Locate and identify every blood parasite.
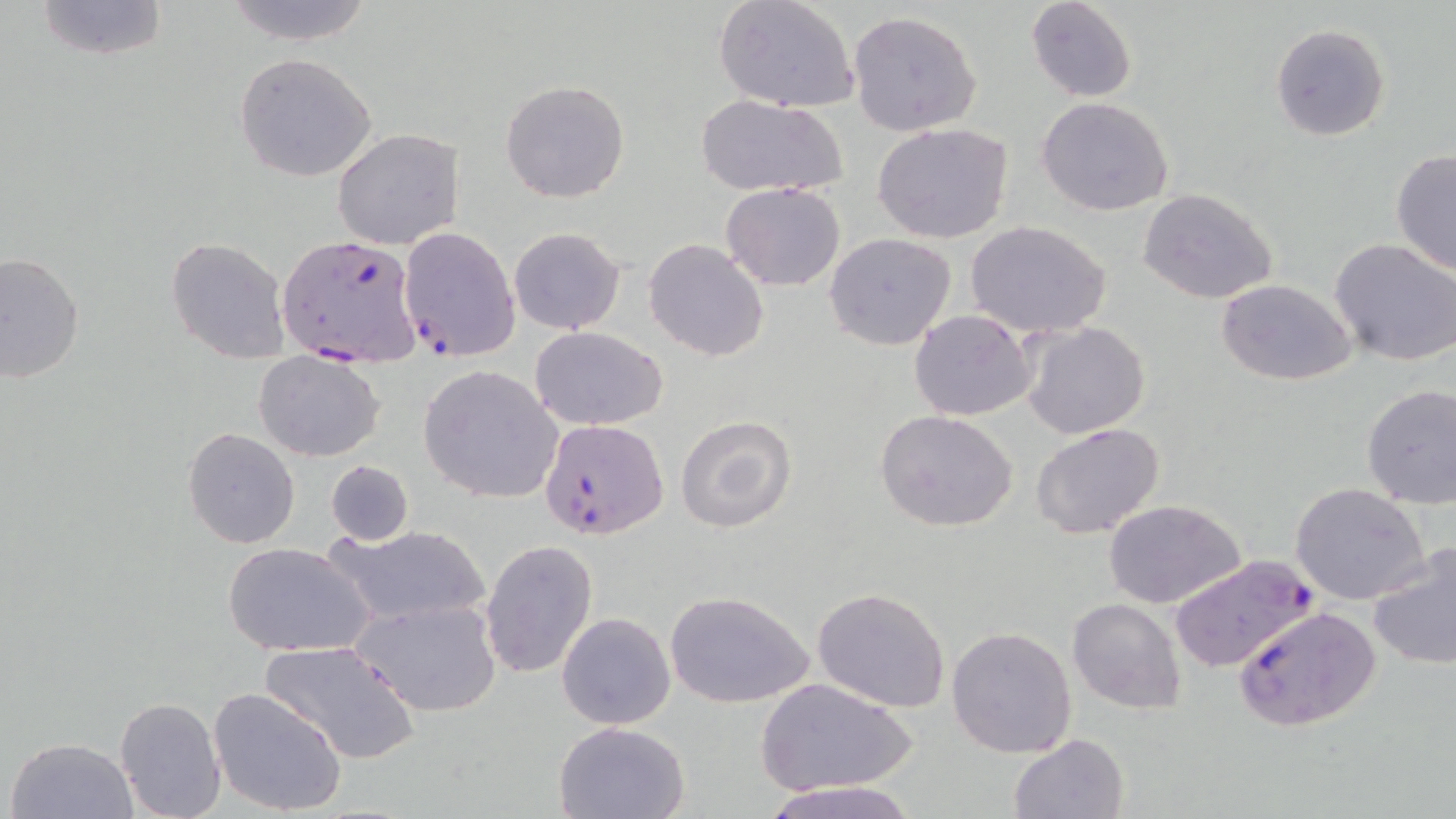
Approximate bounding boxes as named x1/y1/x2/y2 corners in pixels.
Plasmodium falciparum-infected red blood cells: (x1=397, y1=226, x2=520, y2=359), (x1=275, y1=235, x2=419, y2=360), (x1=540, y1=418, x2=669, y2=541), (x1=1167, y1=555, x2=1313, y2=673), (x1=1233, y1=604, x2=1382, y2=736).
No Plasmodium ovale, Plasmodium malariae, Plasmodium vivax, Babesia divergens, or Trypanosoma brucei observed.

Uninfected red blood cell locations: (x1=32, y1=0, x2=169, y2=61), (x1=219, y1=0, x2=379, y2=46), (x1=1025, y1=0, x2=1138, y2=102), (x1=715, y1=1, x2=860, y2=113), (x1=848, y1=10, x2=983, y2=135), (x1=1270, y1=23, x2=1391, y2=140), (x1=233, y1=52, x2=378, y2=182), (x1=500, y1=80, x2=630, y2=203), (x1=696, y1=95, x2=847, y2=199), (x1=1036, y1=96, x2=1174, y2=216), (x1=872, y1=124, x2=1015, y2=245), (x1=332, y1=127, x2=463, y2=248), (x1=1390, y1=150, x2=1455, y2=275), (x1=721, y1=182, x2=845, y2=291), (x1=1136, y1=188, x2=1281, y2=307), (x1=965, y1=219, x2=1113, y2=340), (x1=509, y1=227, x2=626, y2=335), (x1=825, y1=233, x2=958, y2=351), (x1=166, y1=236, x2=290, y2=363), (x1=1329, y1=238, x2=1456, y2=368), (x1=644, y1=239, x2=768, y2=361), (x1=0, y1=252, x2=84, y2=387), (x1=1215, y1=279, x2=1359, y2=385), (x1=908, y1=310, x2=1037, y2=421), (x1=1019, y1=320, x2=1151, y2=440), (x1=531, y1=327, x2=668, y2=430), (x1=255, y1=352, x2=384, y2=460), (x1=420, y1=365, x2=565, y2=504), (x1=1360, y1=384, x2=1456, y2=509), (x1=874, y1=409, x2=1021, y2=534), (x1=675, y1=415, x2=797, y2=532), (x1=1031, y1=421, x2=1166, y2=539), (x1=183, y1=427, x2=300, y2=548), (x1=325, y1=459, x2=412, y2=547), (x1=1290, y1=483, x2=1430, y2=605), (x1=1103, y1=498, x2=1248, y2=607), (x1=329, y1=524, x2=490, y2=627), (x1=479, y1=539, x2=598, y2=679), (x1=1368, y1=539, x2=1456, y2=671), (x1=223, y1=542, x2=375, y2=658), (x1=810, y1=587, x2=952, y2=714), (x1=664, y1=590, x2=813, y2=710), (x1=353, y1=597, x2=502, y2=716), (x1=1067, y1=598, x2=1186, y2=715), (x1=556, y1=611, x2=677, y2=730), (x1=946, y1=626, x2=1078, y2=759), (x1=260, y1=638, x2=420, y2=764), (x1=754, y1=675, x2=918, y2=796), (x1=208, y1=686, x2=348, y2=817), (x1=114, y1=696, x2=227, y2=819), (x1=554, y1=721, x2=692, y2=819), (x1=1009, y1=733, x2=1129, y2=818), (x1=6, y1=736, x2=139, y2=819), (x1=760, y1=780, x2=923, y2=819). Slide-level diagnosis: Plasmodium falciparum. One field of a larger specimen. Image is 1456×819 pixels. Optical microscopy. Thin blood smear. 1000x magnification. May-Grünwald-Giemsa-stained preparation.